Assess this cell for malaria.
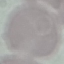
It is uninfected.

Cell patch, automatically extracted from a larger field of view and resized to 64 × 64 pixels. Giemsa-stained preparation. Thin blood smear. Photographed with a smartphone camera at the microscope eyepiece.